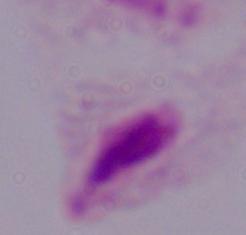
Summary:
  - Modality: photomicrograph
  - Magnification: 1000x
  - Identification: trichomonad